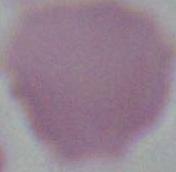

modality: micrograph
magnification: 1000x
identification: erythrocyte